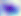 Toxoplasma gondii is seen. Captured at 400x magnification. Micrograph.